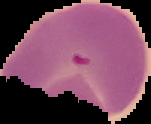

Image is 151×124 pixels. Malaria status: parasitized. From a thin blood smear. Segmented cell region on a black background.